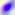

Micrograph. Captured at 400x magnification. Toxoplasma gondii is shown.